Give the extent of all Plasmodium malariae-infected red blood cells.
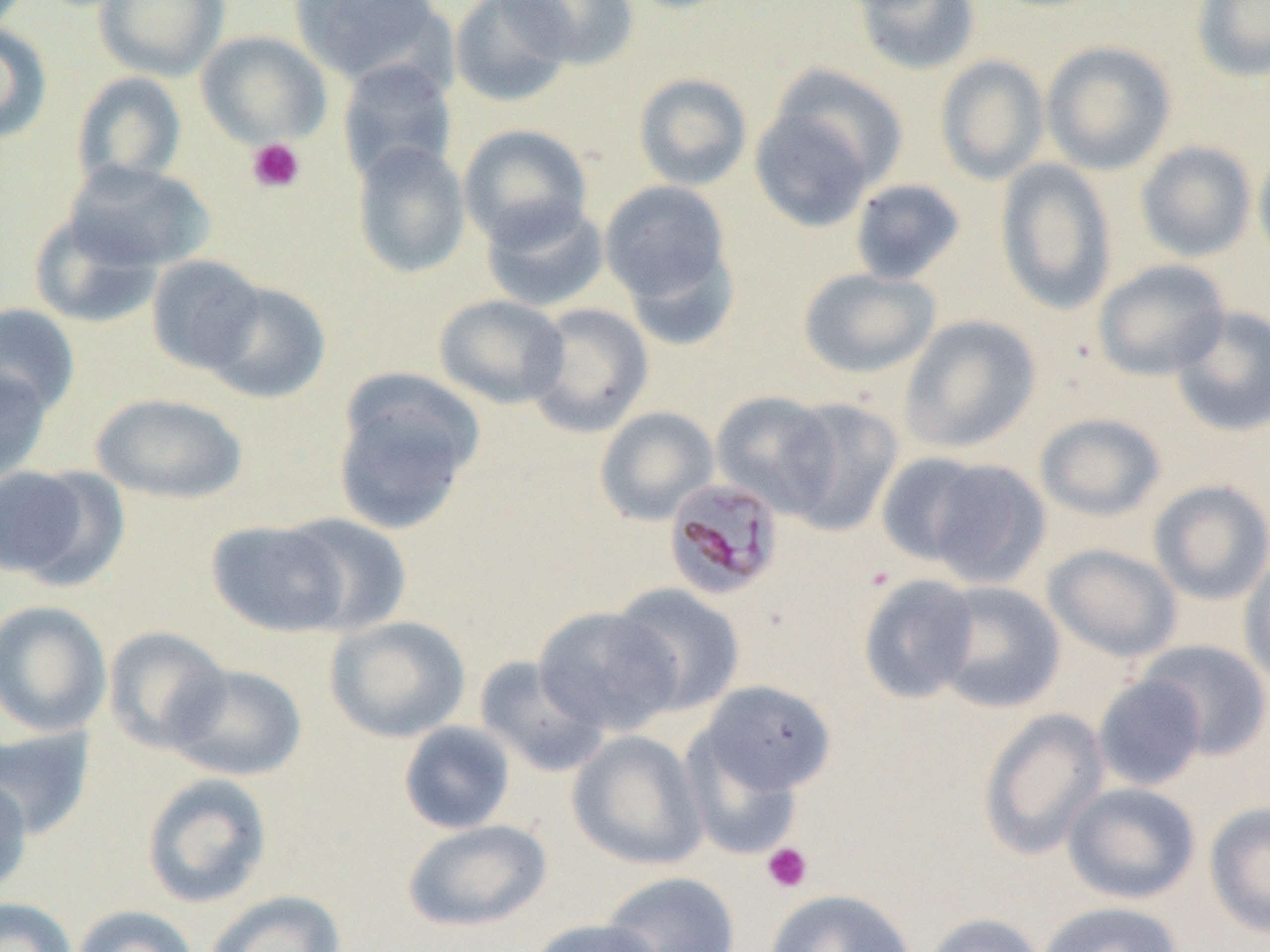
Approximate bounding boxes as [x1, y1, x2, y2] in pixels.
Plasmodium malariae-infected red blood cells: [663, 476, 784, 599].

Summary:
  - Platelet locations: [247, 138, 306, 194], [761, 842, 813, 894]
  - Uninfected red blood cell locations: [94, 0, 228, 81], [289, 0, 448, 87], [449, 0, 575, 107], [500, 0, 639, 69], [1191, 0, 1270, 82], [850, 1, 981, 76], [0, 22, 53, 144], [195, 30, 331, 148], [1040, 41, 1176, 175], [934, 55, 1050, 185], [337, 59, 457, 186], [764, 63, 910, 194], [72, 71, 187, 191], [633, 72, 753, 191], [748, 104, 880, 233], [458, 123, 593, 248], [1135, 140, 1257, 262], [351, 141, 471, 279], [1253, 146, 1270, 271], [994, 159, 1118, 315], [63, 160, 214, 272], [848, 178, 967, 285], [599, 180, 734, 313], [480, 197, 610, 313], [28, 210, 163, 328], [147, 254, 266, 375], [1092, 259, 1231, 381], [797, 267, 941, 379], [201, 280, 332, 405], [434, 294, 569, 409], [522, 302, 654, 438], [0, 303, 80, 417], [1168, 305, 1270, 437], [899, 314, 1041, 454], [0, 365, 53, 485], [331, 370, 484, 535], [711, 390, 841, 516], [90, 393, 248, 504], [778, 397, 902, 535], [594, 406, 719, 525], [1034, 412, 1167, 522], [875, 452, 991, 567], [924, 459, 1051, 588], [0, 463, 117, 587], [1149, 479, 1270, 605], [280, 513, 411, 636], [207, 519, 351, 637], [1043, 543, 1183, 662], [1239, 558, 1270, 690], [857, 574, 980, 705], [931, 581, 1065, 715], [609, 584, 746, 717], [0, 600, 113, 737], [534, 605, 681, 736], [324, 615, 471, 743], [102, 626, 231, 754], [1136, 640, 1270, 761], [474, 655, 610, 778], [166, 663, 307, 782], [1093, 674, 1207, 791], [698, 680, 838, 798], [977, 708, 1110, 860], [398, 721, 516, 834], [0, 726, 95, 840], [567, 730, 709, 871], [680, 730, 806, 861], [141, 772, 273, 909], [0, 776, 32, 898], [1062, 781, 1201, 904], [1204, 802, 1270, 938], [402, 818, 554, 932], [600, 871, 740, 952], [765, 889, 917, 952], [204, 890, 347, 952], [0, 897, 78, 952], [1037, 901, 1184, 952], [71, 905, 199, 952], [920, 913, 1047, 952], [527, 918, 666, 952]
  - Slide-level diagnosis: Plasmodium malariae
  - Field of view: single
  - Modality: light microscopy
  - Image size: 1270×952 pixels
  - Magnification: 1000x
  - Preparation: thin blood film